Assess this cell for malaria.
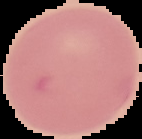

It is uninfected.

Image is 142×139 pixels. Segmented cell region on a black background. From a thin blood smear.